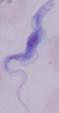 A trypanosome is shown. Micrograph. 1000x magnification.